Assess for malaria.
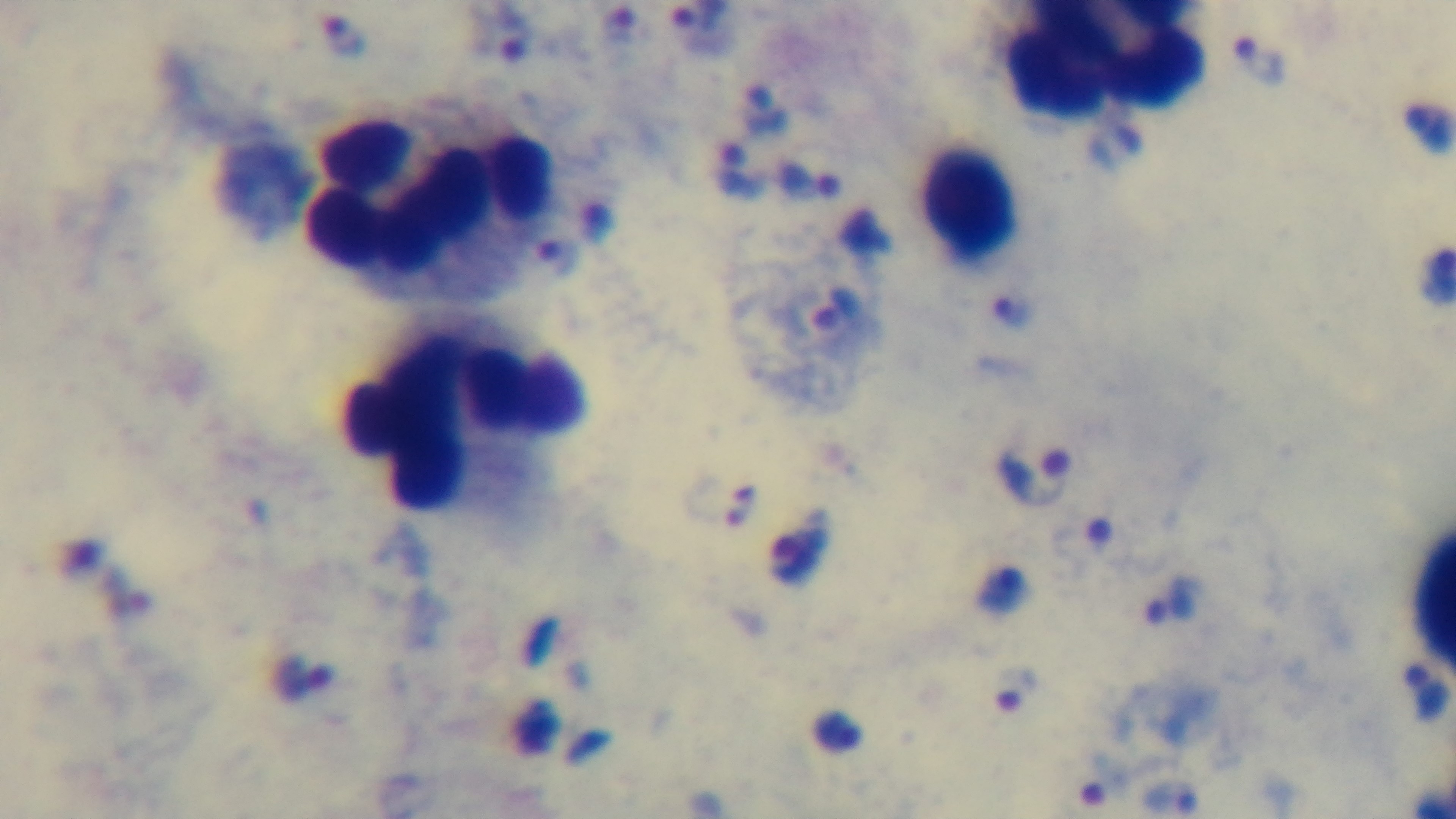
It is infected.

Summary:
  - Field of view: one from the slide
  - Stain: Giemsa
  - Objective: 100x oil immersion
  - Capture: mounted 4K digital camera
  - Modality: light microscopy
  - Preparation: thick